Comment on the morphology of the red blood cells.
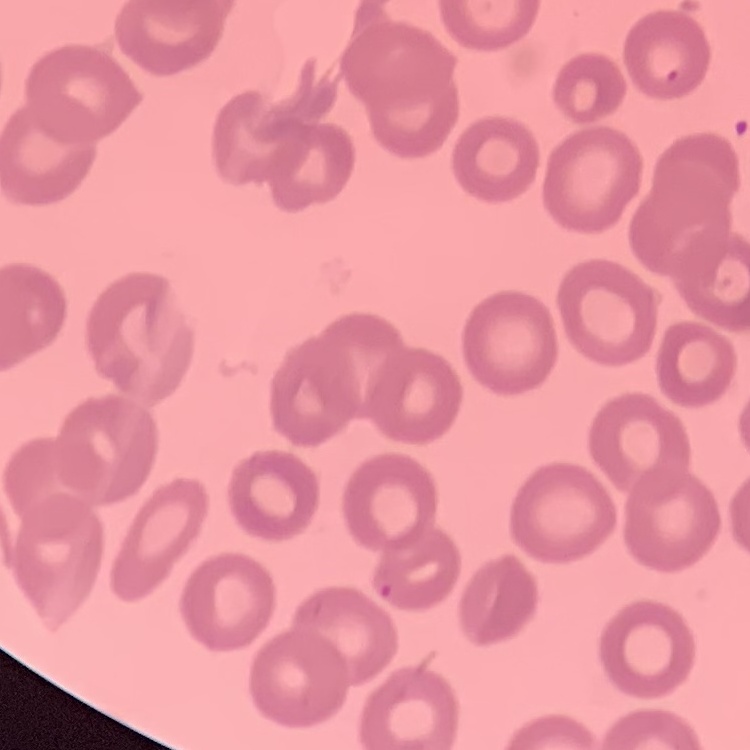

They show no rouleaux formation.

image type = one tile cut from a larger photomicrograph
stain = Field's or Giemsa
preparation = thin blood smear